Locate every blood parasite and identify its species.
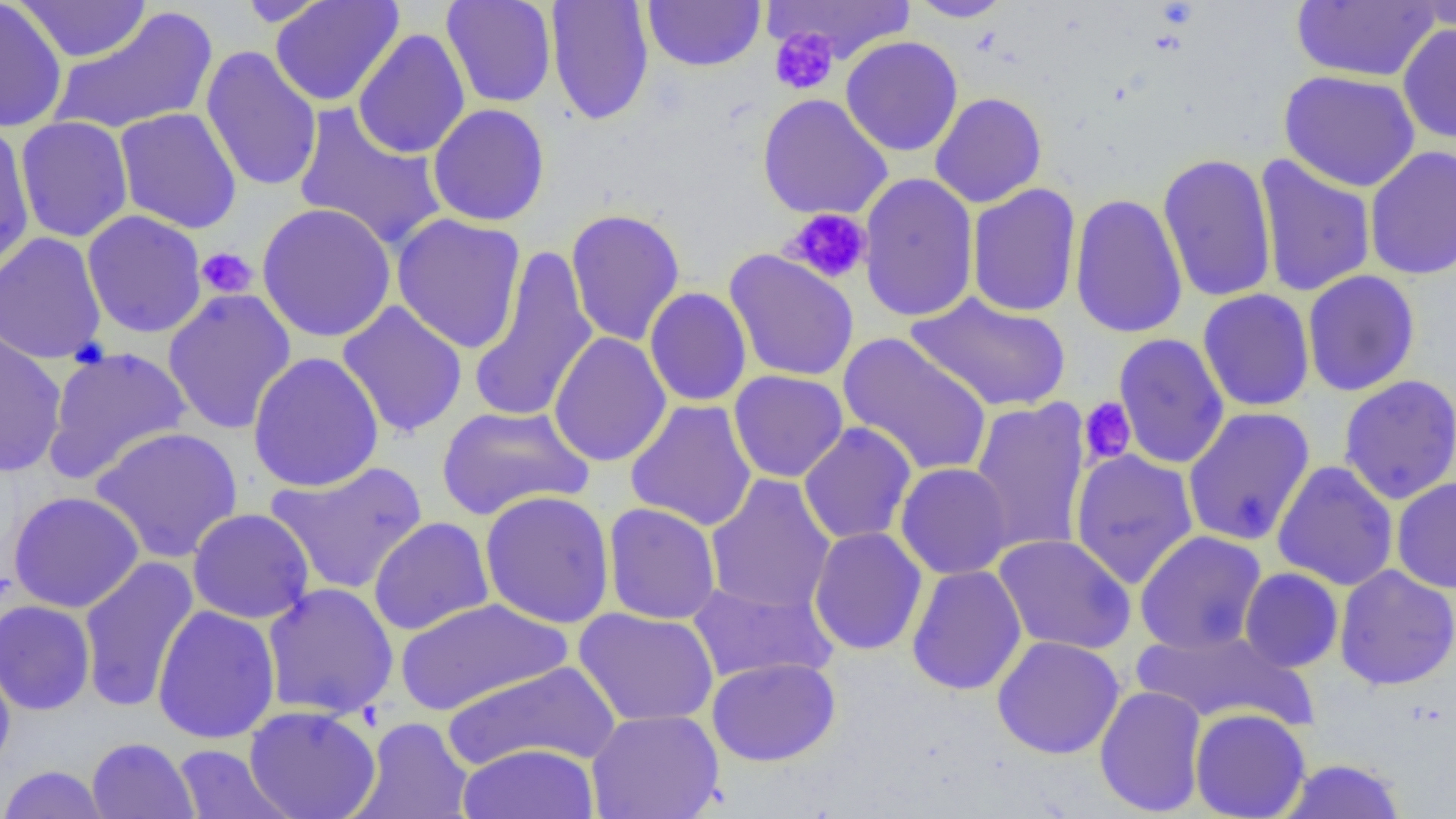

No blood parasites seen.

Approximate bounding boxes as [x1, y1, x2, y2] in pixels. Platelet locations: [770, 29, 838, 96], [782, 208, 872, 285], [196, 247, 258, 299], [1078, 397, 1137, 466]. Uninfected red blood cell locations: [0, 0, 68, 133], [270, 0, 405, 107], [441, 0, 557, 108], [546, 0, 654, 126], [764, 0, 916, 65], [907, 0, 1015, 22], [1410, 0, 1456, 36], [15, 1, 152, 63], [235, 1, 336, 27], [643, 1, 766, 71], [1291, 1, 1441, 83], [48, 7, 218, 137], [1397, 23, 1456, 144], [352, 28, 471, 160], [840, 35, 963, 156], [200, 45, 322, 193], [1278, 69, 1421, 192], [930, 92, 1047, 208], [757, 93, 893, 220], [293, 103, 447, 252], [427, 104, 550, 227], [114, 107, 242, 234], [15, 116, 134, 243], [0, 120, 35, 279], [1364, 146, 1456, 281], [1157, 152, 1277, 304], [1254, 154, 1377, 297], [858, 172, 979, 323], [966, 183, 1082, 318], [1069, 192, 1188, 339], [256, 202, 397, 343], [566, 208, 686, 346], [82, 210, 207, 339], [391, 213, 527, 354], [0, 232, 107, 364], [467, 245, 599, 423], [724, 249, 859, 383], [1302, 270, 1421, 397], [644, 287, 752, 407], [162, 288, 298, 435], [1197, 289, 1315, 412], [906, 292, 1072, 413], [336, 301, 468, 439], [0, 326, 67, 478], [548, 332, 672, 467], [838, 332, 992, 478], [1112, 333, 1230, 469], [41, 345, 193, 485], [247, 351, 385, 493], [728, 370, 848, 483], [1338, 374, 1456, 505], [624, 399, 758, 532], [968, 399, 1091, 554], [436, 404, 593, 521], [1182, 407, 1316, 546], [798, 421, 917, 546], [89, 426, 243, 564], [1070, 449, 1199, 589], [266, 460, 429, 596], [1272, 461, 1399, 591], [894, 462, 1014, 580], [704, 473, 836, 616], [1391, 477, 1456, 593], [479, 489, 615, 629], [8, 491, 144, 613], [603, 502, 721, 625], [187, 508, 315, 624], [368, 517, 495, 636], [808, 526, 928, 656], [1134, 530, 1267, 654], [993, 534, 1136, 655], [78, 556, 199, 712], [1334, 564, 1456, 691], [906, 565, 1028, 695], [1239, 567, 1344, 672], [686, 579, 836, 684], [262, 582, 399, 720], [394, 597, 572, 716], [0, 599, 96, 715], [152, 605, 281, 744], [573, 607, 719, 727], [1130, 627, 1314, 728], [992, 635, 1125, 759], [0, 650, 16, 776], [706, 657, 841, 766], [440, 660, 621, 773], [1094, 685, 1208, 817], [244, 705, 381, 818], [1190, 708, 1311, 818], [585, 709, 724, 819], [351, 716, 475, 818], [86, 737, 198, 819], [457, 742, 599, 818], [172, 744, 293, 819], [1276, 759, 1408, 819], [0, 765, 111, 819]. Slide-level diagnosis: negative for blood parasites. Thin blood film. One field of a larger specimen. Optical microscopy. Captured at 1000x magnification. Image is 1456×819 pixels.